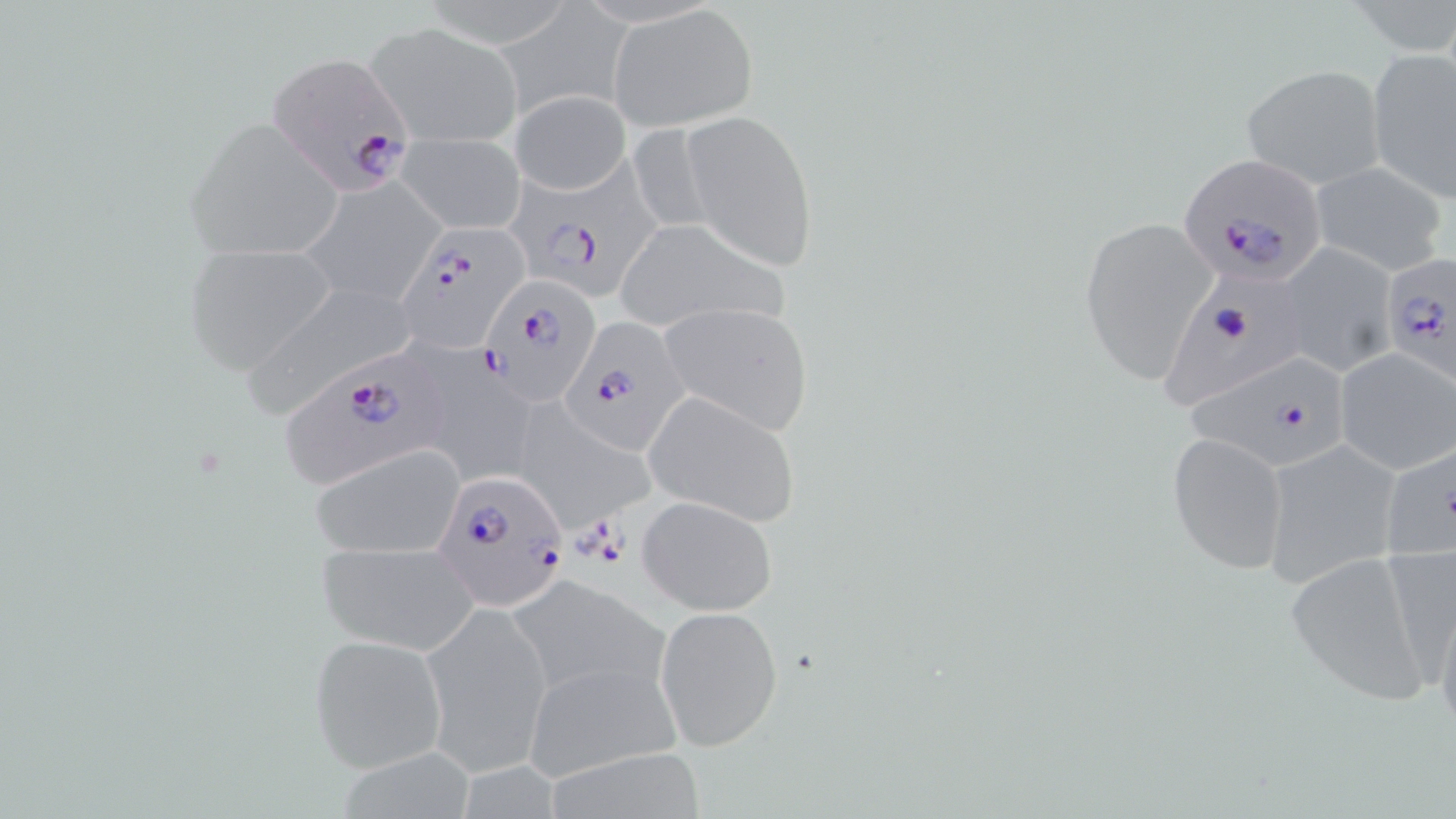

Summary:
  - Coordinate format: approximate bounding boxes as [x1, y1, x2, y2] in pixels
  - Plasmodium falciparum-infected red blood cell locations: [265, 50, 417, 197], [1179, 156, 1331, 287], [505, 165, 660, 300], [389, 226, 527, 353], [1378, 254, 1454, 382], [1161, 268, 1308, 416], [478, 276, 602, 405], [559, 316, 692, 453], [280, 347, 461, 489], [1186, 352, 1352, 472], [434, 470, 567, 610]
  - Uninfected red blood cell locations: [610, 6, 758, 130], [364, 20, 522, 148], [1365, 46, 1456, 207], [1240, 63, 1387, 190], [510, 90, 631, 195], [682, 109, 819, 272], [183, 119, 348, 263], [398, 135, 527, 234], [1309, 161, 1448, 276], [300, 175, 443, 309], [1079, 213, 1220, 383], [613, 219, 792, 334], [182, 243, 338, 372], [1280, 243, 1397, 377], [237, 279, 425, 416], [656, 302, 814, 435], [1333, 346, 1456, 474], [419, 359, 540, 489], [643, 390, 801, 527], [512, 401, 659, 531], [1168, 431, 1290, 576], [1260, 438, 1405, 591], [1379, 441, 1455, 566], [311, 445, 466, 560], [637, 495, 779, 615], [1375, 538, 1456, 687], [317, 539, 477, 654], [1284, 551, 1436, 703], [508, 575, 668, 701], [1432, 591, 1456, 738], [421, 604, 552, 774], [654, 605, 783, 750], [307, 633, 449, 773], [520, 659, 682, 784]
  - Slide-level diagnosis: Plasmodium falciparum
  - Modality: optical microscopy
  - Image size: 1456×819 pixels
  - Field of view: single
  - Magnification: 1000x
  - Stain: May-Grünwald-Giemsa
  - Preparation: thin blood film